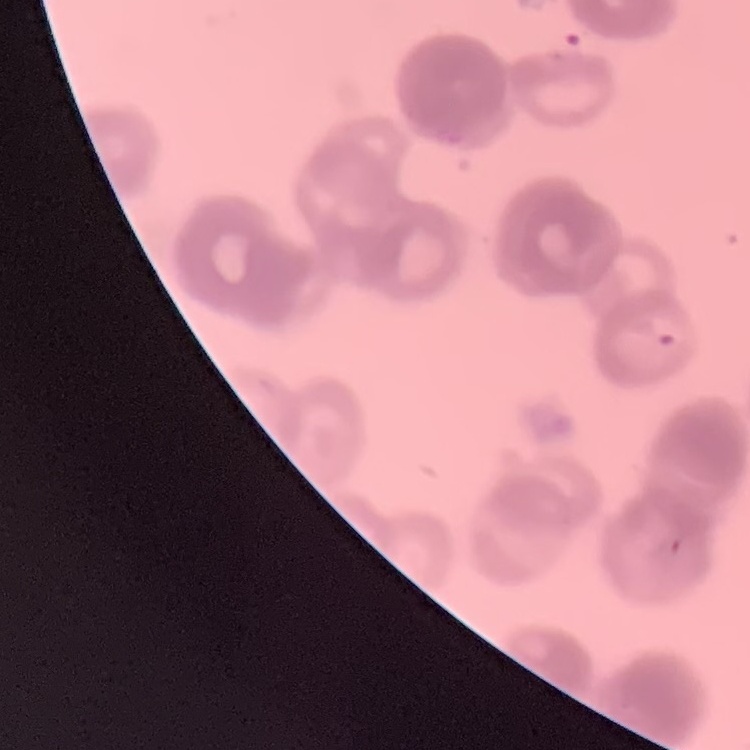
erythrocyte_morphology: rouleaux formation
preparation: thin blood film
image_type: one tile cut from a larger photomicrograph
stain: Field's or Giemsa